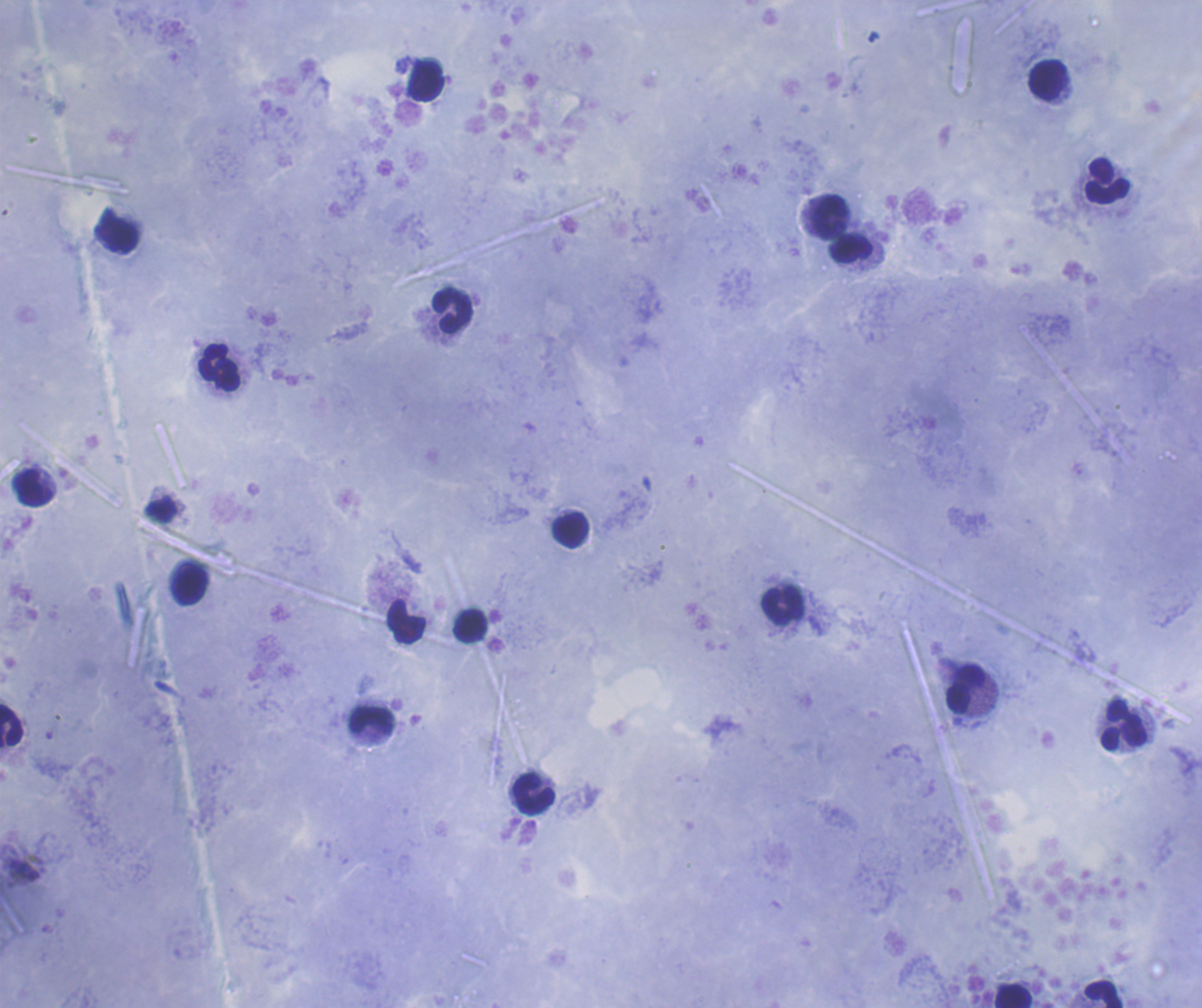
Approximate centers as {x, y} in pixels.
Summary:
  - Leukocyte locations: {1047, 80}, {426, 81}, {1107, 181}, {829, 217}, {118, 235}, {851, 249}, {452, 311}, {218, 368}, {33, 489}, {570, 530}, {190, 584}, {782, 605}, {406, 621}, {469, 625}, {966, 689}, {372, 721}, {11, 726}, {1124, 726}, {534, 794}, {1103, 994}, {1013, 995}
  - Coloration quality: good
  - Result: no Plasmodium parasites seen
  - Preparation: thick blood film
  - Magnification: 100x
  - Background quality: satisfactory
  - Stain: Romanowsky
  - Image size: 1202×1008 pixels
  - Field of view: single
  - Context: previously used in a real diagnosis